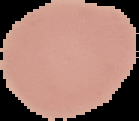 Segmented cell region on a black background. Malaria status: uninfected. From a thin blood film. Image is 139×121 pixels.